Identify the cell.
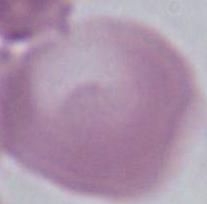

This is an erythrocyte.

magnification = 1000x
modality = photomicrograph